Classify this cell by malaria status.
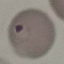

Parasitized.

Acquired by smartphone through the microscope eyepiece. Thin smear of blood. Automatically extracted cell patch, resized to 64 × 64 pixels. Giemsa stain.